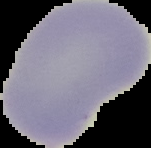

Segmented cell region on a black background. Result: negative for Plasmodium parasites. From a thin blood smear. Image is 151×148 pixels.